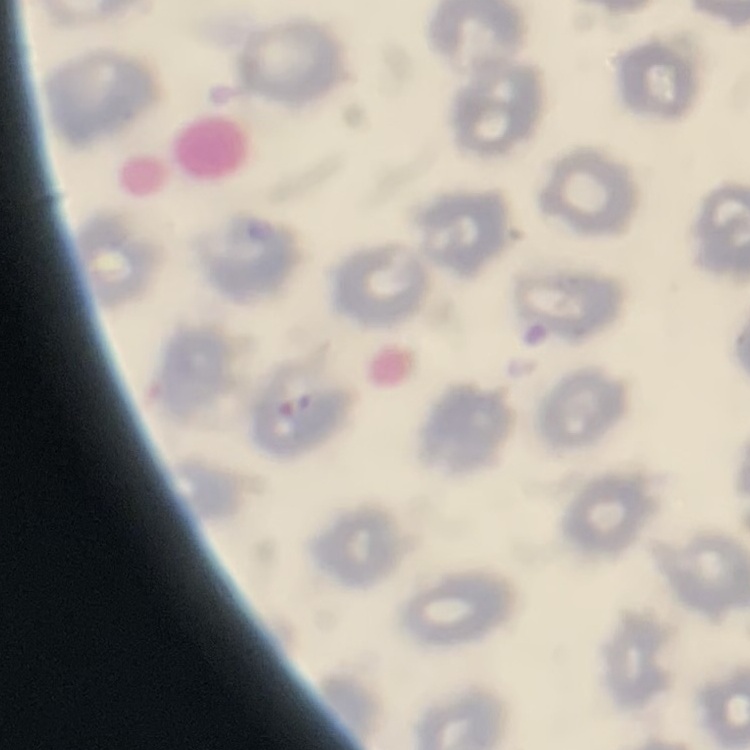
The red blood cells exhibit no rouleaux formation. Field's or Giemsa stain. Thin blood film. One tile cut from a larger photomicrograph.